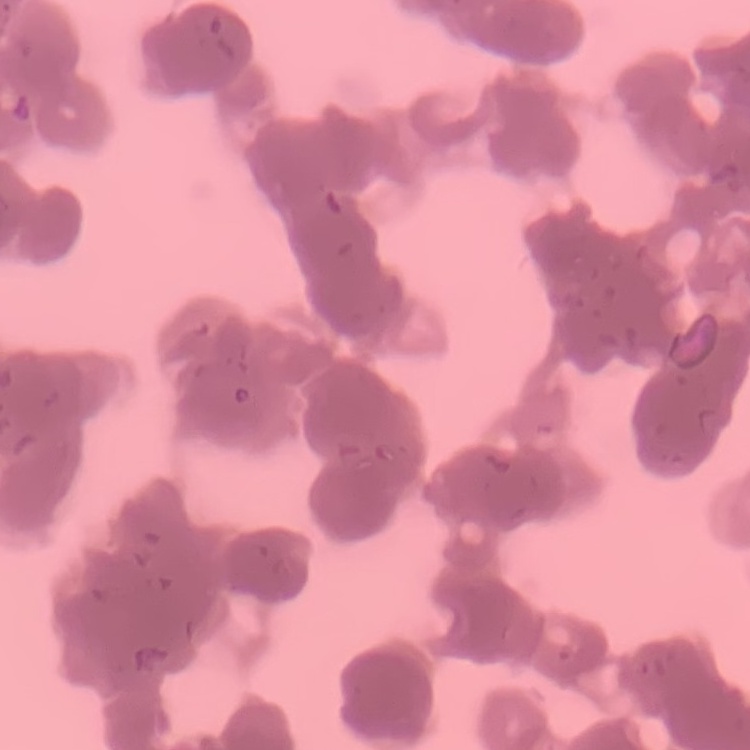
The erythrocytes show rouleaux formation. Thin blood film. One tile cut from a larger photomicrograph. Stained with either Field's or Giemsa.